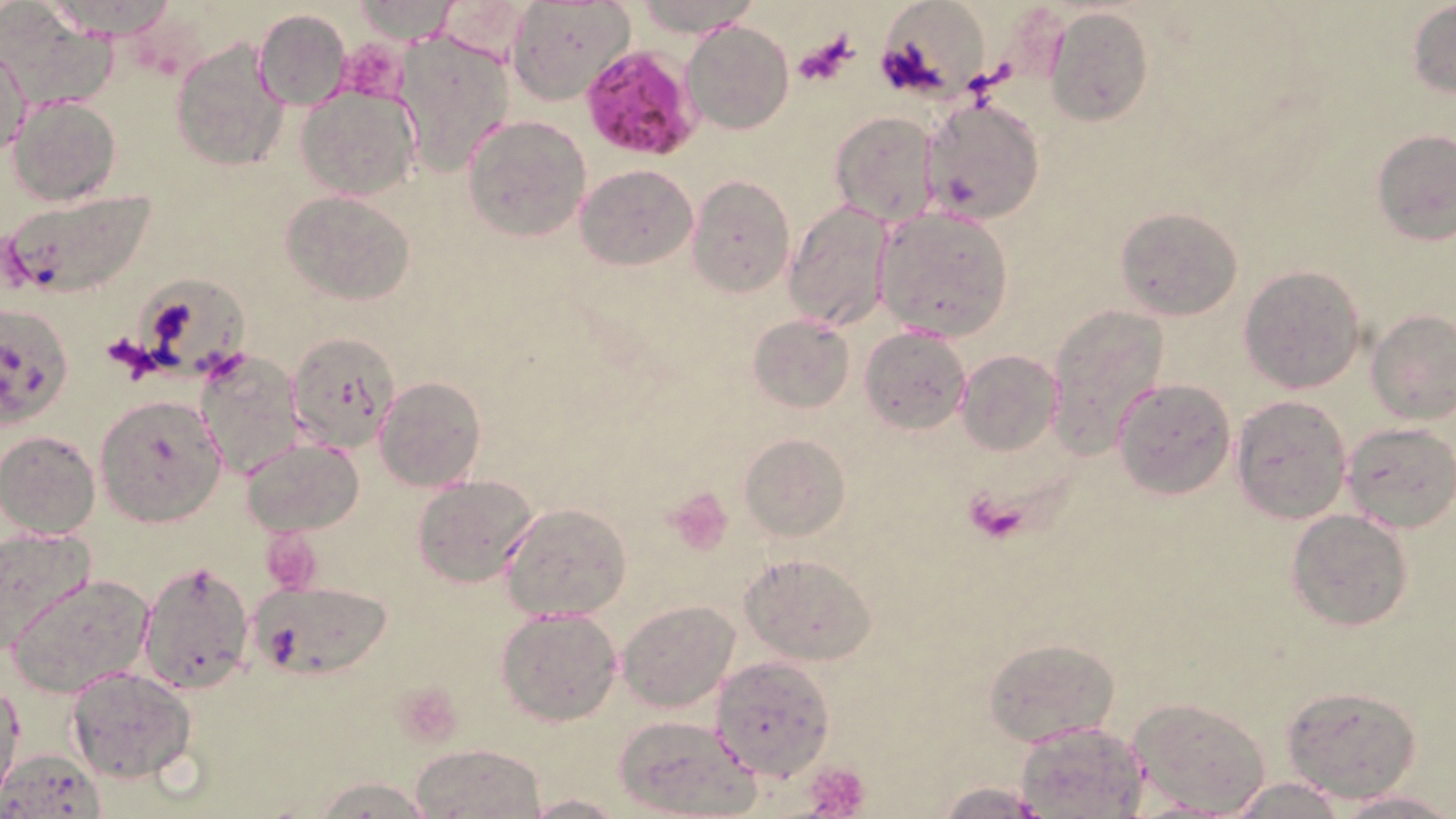
Approximate bounding boxes as named x1/y1/x2/y2 corners in pixels. Plasmodium falciparum-infected red blood cell locations: (x1=578, y1=47, x2=701, y2=161). Platelet locations: (x1=794, y1=33, x2=856, y2=87), (x1=336, y1=42, x2=410, y2=102), (x1=963, y1=487, x2=1030, y2=546), (x1=665, y1=488, x2=734, y2=557), (x1=263, y1=530, x2=324, y2=591), (x1=393, y1=683, x2=466, y2=747), (x1=806, y1=760, x2=872, y2=818). Uninfected red blood cell locations: (x1=350, y1=0, x2=460, y2=44), (x1=507, y1=0, x2=636, y2=104), (x1=630, y1=0, x2=763, y2=36), (x1=6, y1=3, x2=117, y2=110), (x1=1407, y1=3, x2=1455, y2=98), (x1=877, y1=4, x2=991, y2=107), (x1=1044, y1=6, x2=1152, y2=127), (x1=253, y1=8, x2=350, y2=110), (x1=684, y1=20, x2=793, y2=134), (x1=394, y1=30, x2=515, y2=177), (x1=170, y1=35, x2=289, y2=173), (x1=1, y1=40, x2=31, y2=157), (x1=296, y1=86, x2=421, y2=201), (x1=8, y1=95, x2=121, y2=206), (x1=920, y1=98, x2=1046, y2=224), (x1=830, y1=111, x2=941, y2=225), (x1=463, y1=114, x2=591, y2=243), (x1=1370, y1=130, x2=1455, y2=245), (x1=576, y1=164, x2=698, y2=271), (x1=688, y1=176, x2=794, y2=297), (x1=1, y1=186, x2=160, y2=301), (x1=282, y1=191, x2=416, y2=305), (x1=782, y1=200, x2=892, y2=331), (x1=1115, y1=206, x2=1243, y2=320), (x1=874, y1=207, x2=1014, y2=340), (x1=1238, y1=265, x2=1367, y2=393), (x1=133, y1=276, x2=259, y2=390), (x1=0, y1=301, x2=73, y2=426), (x1=1044, y1=303, x2=1170, y2=460), (x1=1367, y1=308, x2=1456, y2=424), (x1=748, y1=314, x2=856, y2=414), (x1=860, y1=326, x2=972, y2=435), (x1=287, y1=333, x2=403, y2=453), (x1=196, y1=350, x2=305, y2=481), (x1=956, y1=350, x2=1061, y2=457), (x1=374, y1=376, x2=486, y2=493), (x1=1112, y1=378, x2=1237, y2=498), (x1=95, y1=394, x2=226, y2=525), (x1=1230, y1=395, x2=1353, y2=523), (x1=1340, y1=422, x2=1456, y2=534), (x1=0, y1=430, x2=101, y2=539), (x1=739, y1=433, x2=849, y2=542), (x1=242, y1=438, x2=364, y2=536), (x1=413, y1=474, x2=543, y2=588), (x1=500, y1=501, x2=632, y2=622), (x1=1286, y1=508, x2=1415, y2=630), (x1=0, y1=526, x2=95, y2=655), (x1=741, y1=552, x2=878, y2=666), (x1=134, y1=557, x2=255, y2=693), (x1=9, y1=571, x2=155, y2=697), (x1=244, y1=579, x2=394, y2=682), (x1=616, y1=600, x2=739, y2=713), (x1=495, y1=608, x2=624, y2=726), (x1=983, y1=636, x2=1119, y2=746), (x1=711, y1=655, x2=836, y2=781), (x1=65, y1=666, x2=197, y2=785), (x1=0, y1=680, x2=24, y2=794), (x1=1280, y1=682, x2=1424, y2=803), (x1=1128, y1=698, x2=1273, y2=815), (x1=612, y1=715, x2=760, y2=817), (x1=1016, y1=721, x2=1148, y2=816), (x1=411, y1=743, x2=546, y2=819), (x1=0, y1=748, x2=107, y2=818), (x1=312, y1=776, x2=436, y2=818), (x1=1224, y1=776, x2=1350, y2=818), (x1=930, y1=779, x2=1057, y2=819), (x1=1334, y1=789, x2=1455, y2=818), (x1=525, y1=791, x2=623, y2=818). Slide-level diagnosis: Plasmodium falciparum. Image is 1456×819 pixels. Light microscopy. Thin blood smear. 1000x magnification. Single field of view. May-Grünwald-Giemsa stain.